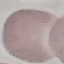
Summary:
  - Malaria status: uninfected
  - Stain: Giemsa
  - Preparation: thin blood film
  - Image type: automatically extracted cell patch, resized to 64 × 64 pixels
  - Capture: smartphone through the microscope eyepiece